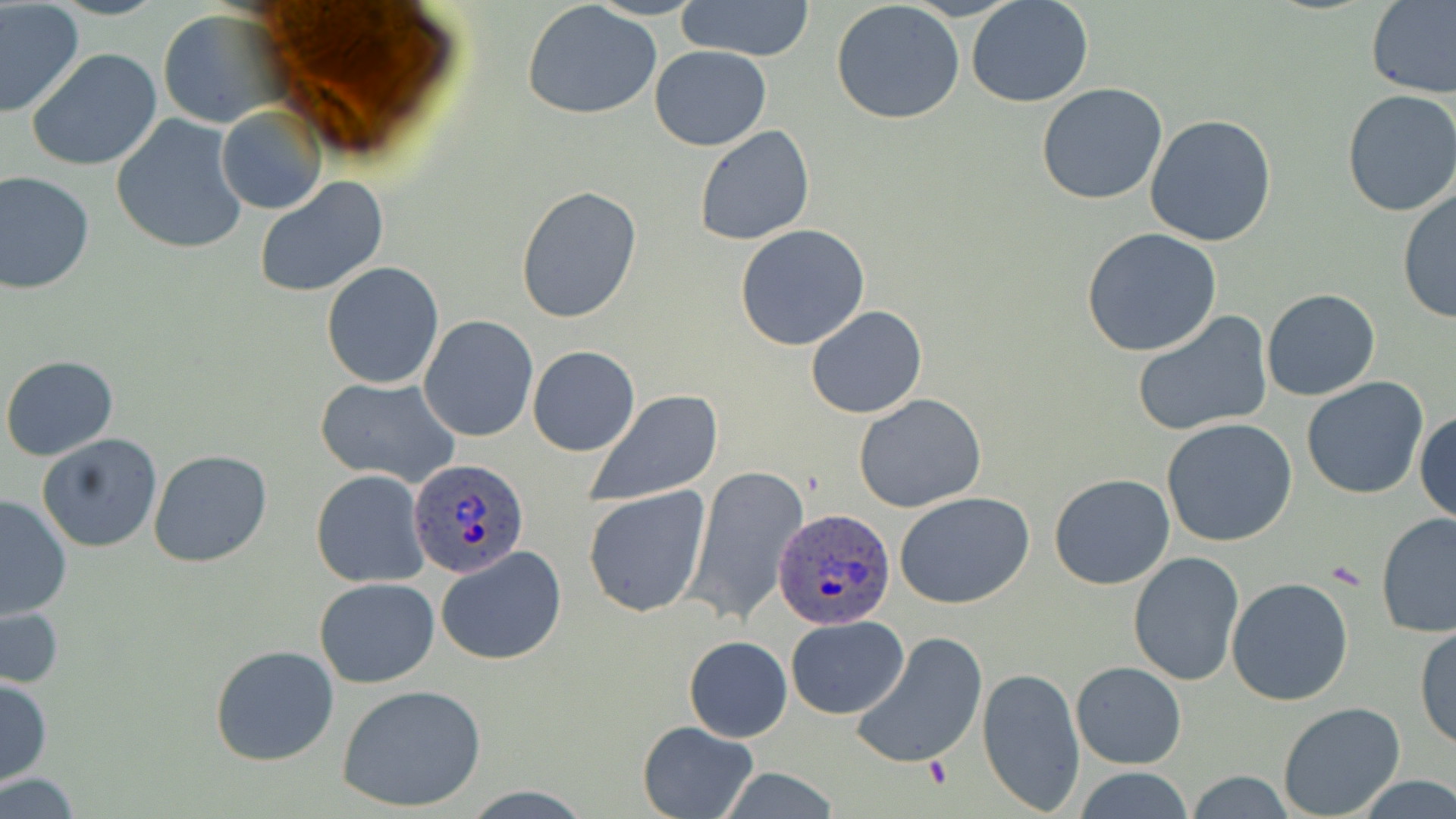

Summary:
  - Coordinate format: approximate bounding boxes as named x1/y1/x2/y2 corners in pixels
  - Uninfected red blood cell locations: (x1=1366, y1=0, x2=1456, y2=100), (x1=678, y1=1, x2=817, y2=60), (x1=831, y1=1, x2=965, y2=124), (x1=965, y1=1, x2=1094, y2=109), (x1=522, y1=2, x2=663, y2=119), (x1=0, y1=3, x2=83, y2=117), (x1=156, y1=9, x2=281, y2=129), (x1=650, y1=45, x2=771, y2=151), (x1=27, y1=48, x2=164, y2=172), (x1=1036, y1=83, x2=1168, y2=205), (x1=1341, y1=91, x2=1456, y2=217), (x1=217, y1=105, x2=326, y2=214), (x1=111, y1=114, x2=248, y2=256), (x1=1145, y1=114, x2=1278, y2=246), (x1=694, y1=124, x2=815, y2=246), (x1=0, y1=171, x2=95, y2=295), (x1=254, y1=177, x2=389, y2=298), (x1=515, y1=186, x2=642, y2=325), (x1=1397, y1=187, x2=1455, y2=323), (x1=734, y1=224, x2=873, y2=352), (x1=1082, y1=228, x2=1223, y2=357), (x1=321, y1=261, x2=446, y2=390), (x1=1261, y1=287, x2=1381, y2=401), (x1=806, y1=305, x2=926, y2=420), (x1=1131, y1=311, x2=1272, y2=436), (x1=419, y1=315, x2=539, y2=443), (x1=528, y1=346, x2=640, y2=457), (x1=1, y1=355, x2=118, y2=461), (x1=541, y1=364, x2=695, y2=485), (x1=315, y1=375, x2=460, y2=490), (x1=1301, y1=376, x2=1430, y2=500), (x1=583, y1=390, x2=725, y2=503), (x1=853, y1=393, x2=986, y2=513), (x1=1414, y1=408, x2=1456, y2=526), (x1=1160, y1=419, x2=1299, y2=547), (x1=37, y1=433, x2=162, y2=553), (x1=148, y1=449, x2=272, y2=568), (x1=684, y1=464, x2=809, y2=627), (x1=309, y1=469, x2=430, y2=589), (x1=1049, y1=474, x2=1175, y2=590), (x1=583, y1=484, x2=712, y2=618), (x1=894, y1=491, x2=1036, y2=609), (x1=0, y1=494, x2=74, y2=621), (x1=1376, y1=512, x2=1456, y2=641), (x1=436, y1=547, x2=567, y2=664), (x1=1128, y1=551, x2=1246, y2=687), (x1=314, y1=577, x2=439, y2=689), (x1=1226, y1=577, x2=1354, y2=705), (x1=1, y1=602, x2=64, y2=692), (x1=785, y1=617, x2=909, y2=719), (x1=1413, y1=622, x2=1456, y2=749), (x1=850, y1=631, x2=988, y2=770), (x1=684, y1=635, x2=793, y2=742), (x1=210, y1=644, x2=340, y2=765), (x1=1071, y1=660, x2=1187, y2=769), (x1=976, y1=666, x2=1084, y2=815), (x1=0, y1=677, x2=52, y2=786), (x1=337, y1=683, x2=487, y2=813), (x1=1276, y1=702, x2=1407, y2=818), (x1=637, y1=720, x2=759, y2=817), (x1=1072, y1=767, x2=1193, y2=819), (x1=1186, y1=771, x2=1296, y2=816), (x1=0, y1=774, x2=84, y2=817), (x1=1358, y1=776, x2=1456, y2=817)
  - Plasmodium ovale-infected red blood cell locations: (x1=409, y1=455, x2=530, y2=576), (x1=774, y1=508, x2=896, y2=632)
  - Slide-level diagnosis: Plasmodium ovale
  - Stain: May-Grünwald-Giemsa
  - Field of view: one of a larger specimen
  - Preparation: thin blood smear
  - Image size: 1456×819 pixels
  - Magnification: 1000x
  - Modality: light microscopy